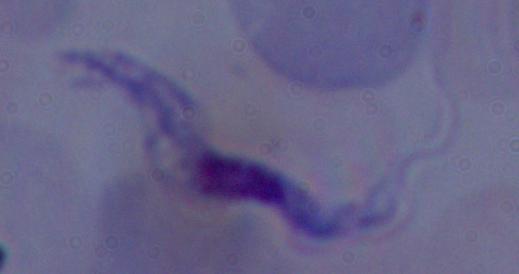

identification = trypanosome
magnification = 1000x
modality = photomicrograph